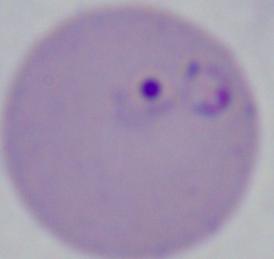
Summary:
  - Identification: Babesia
  - Magnification: 1000x
  - Modality: micrograph